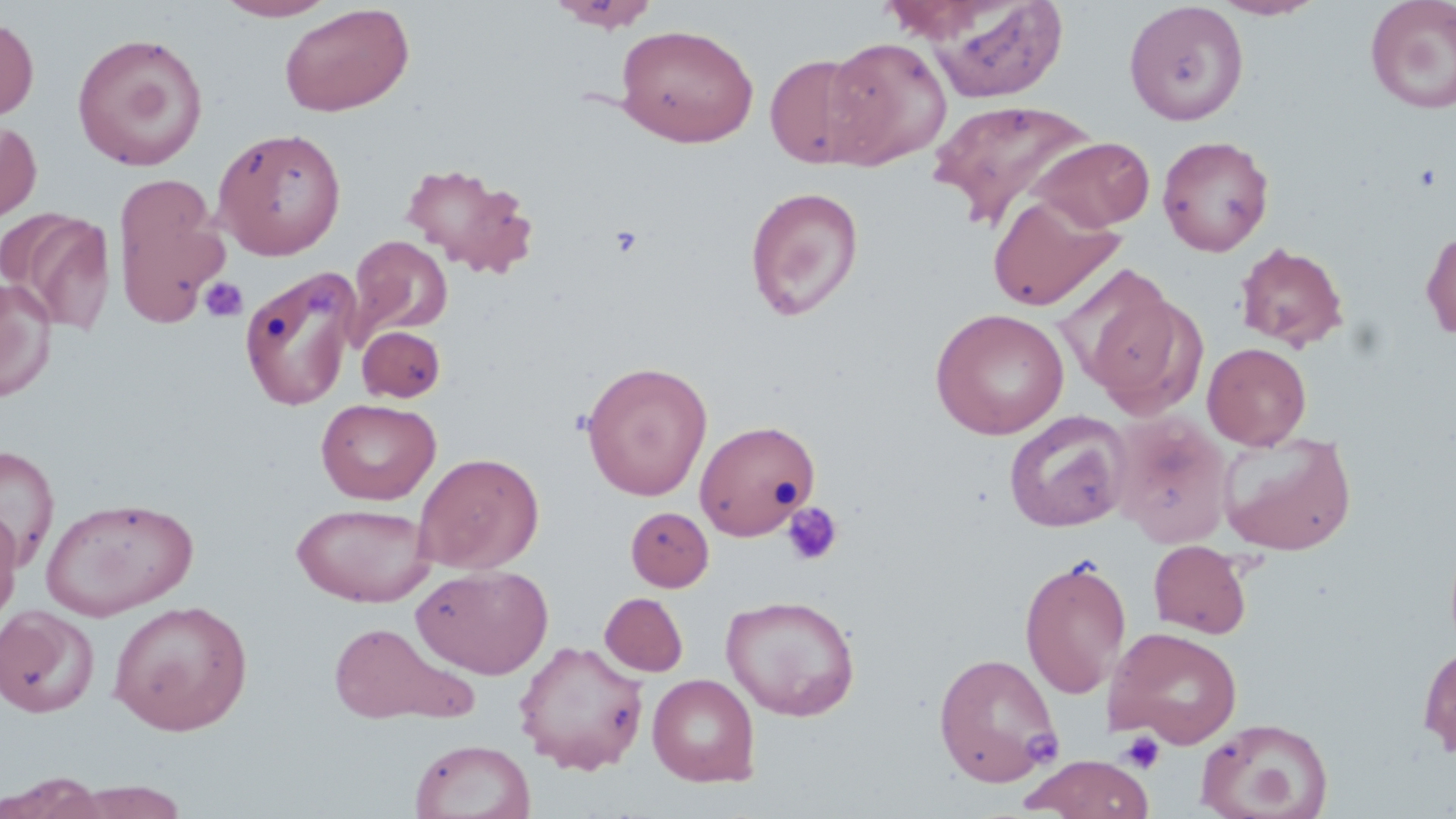
slide-level diagnosis = no evidence of blood parasites
preparation = thin blood film
uninfected red blood cell locations = approximate bounding boxes as [x1, y1, x2, y2] in pixels: [215, 0, 337, 21], [546, 0, 661, 32], [912, 0, 1070, 103], [1209, 0, 1327, 20], [1124, 1, 1249, 126], [1364, 1, 1456, 115], [279, 2, 414, 117], [0, 17, 38, 121], [615, 23, 759, 147], [72, 32, 210, 172], [821, 37, 952, 169], [763, 52, 882, 171], [928, 97, 1096, 230], [0, 119, 42, 222], [213, 126, 348, 260], [1157, 134, 1275, 256], [1027, 136, 1155, 233], [400, 162, 538, 276], [112, 173, 230, 328], [744, 186, 865, 321], [987, 191, 1124, 312], [3, 210, 116, 335], [1420, 227, 1456, 343], [348, 235, 452, 341], [1234, 241, 1349, 351], [239, 267, 363, 411], [0, 278, 56, 401], [1076, 284, 1207, 419], [930, 308, 1070, 439], [357, 325, 446, 402], [1202, 342, 1312, 450], [580, 360, 713, 501], [316, 398, 441, 505], [1002, 410, 1131, 533], [1109, 412, 1235, 548], [694, 419, 821, 540], [1218, 432, 1357, 556], [0, 444, 60, 568], [412, 451, 545, 574], [40, 496, 199, 620], [291, 502, 434, 606], [0, 503, 22, 628], [625, 507, 713, 591], [1149, 540, 1253, 638], [1019, 557, 1131, 699], [411, 563, 553, 680], [600, 592, 688, 676], [720, 593, 860, 721], [109, 600, 253, 736], [0, 604, 100, 718], [328, 622, 466, 724], [1105, 626, 1244, 749], [514, 639, 650, 775], [1417, 642, 1456, 759], [932, 651, 1062, 786], [647, 673, 760, 786], [1196, 716, 1334, 819], [409, 739, 535, 819], [1022, 755, 1154, 819], [2, 773, 109, 819], [65, 781, 190, 819]
image size = 1456×819 pixels
field of view = one of a larger specimen
stain = May-Grünwald-Giemsa
magnification = 1000x
platelet locations = approximate bounding boxes as [x1, y1, x2, y2] in pixels: [1411, 164, 1444, 191], [609, 225, 644, 257], [199, 277, 248, 323], [782, 502, 844, 567], [1119, 731, 1164, 773]
modality = light microscopy